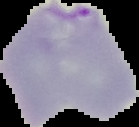

preparation = thin blood smear
image type = cell region segmented out of the field of view; surrounding area masked to black
image size = 139×127 pixels
malaria status = parasitized